Assess the morphology of the erythrocytes.
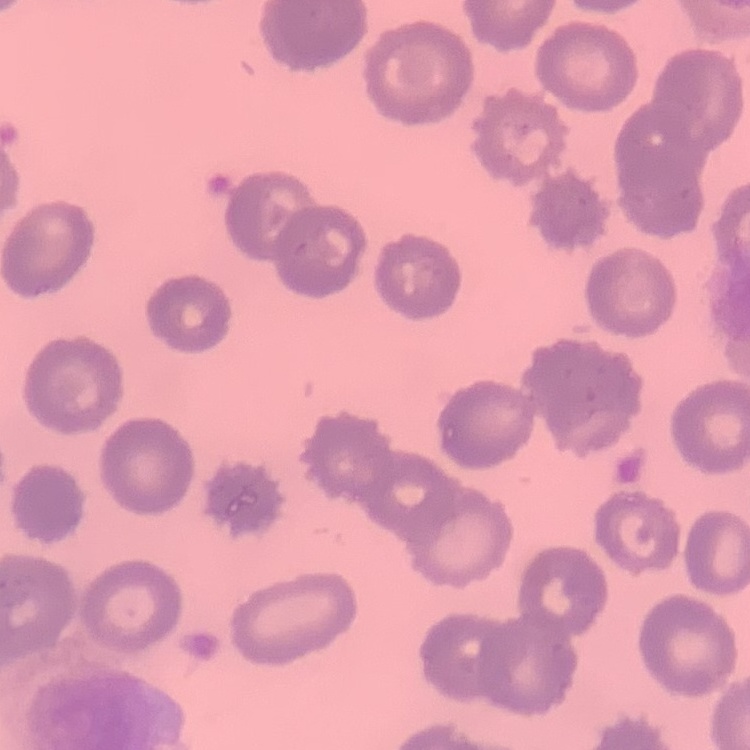

They show no rouleaux formation.

image type = square crop of a larger photomicrograph
stain = Field's or Giemsa
preparation = thin blood film